Classify this cell by malaria status.
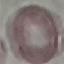
It is uninfected.

Giemsa stain. Cell patch, automatically extracted from a larger field of view and resized to 64 × 64 pixels. Acquired by smartphone through the microscope eyepiece. Thin blood film.